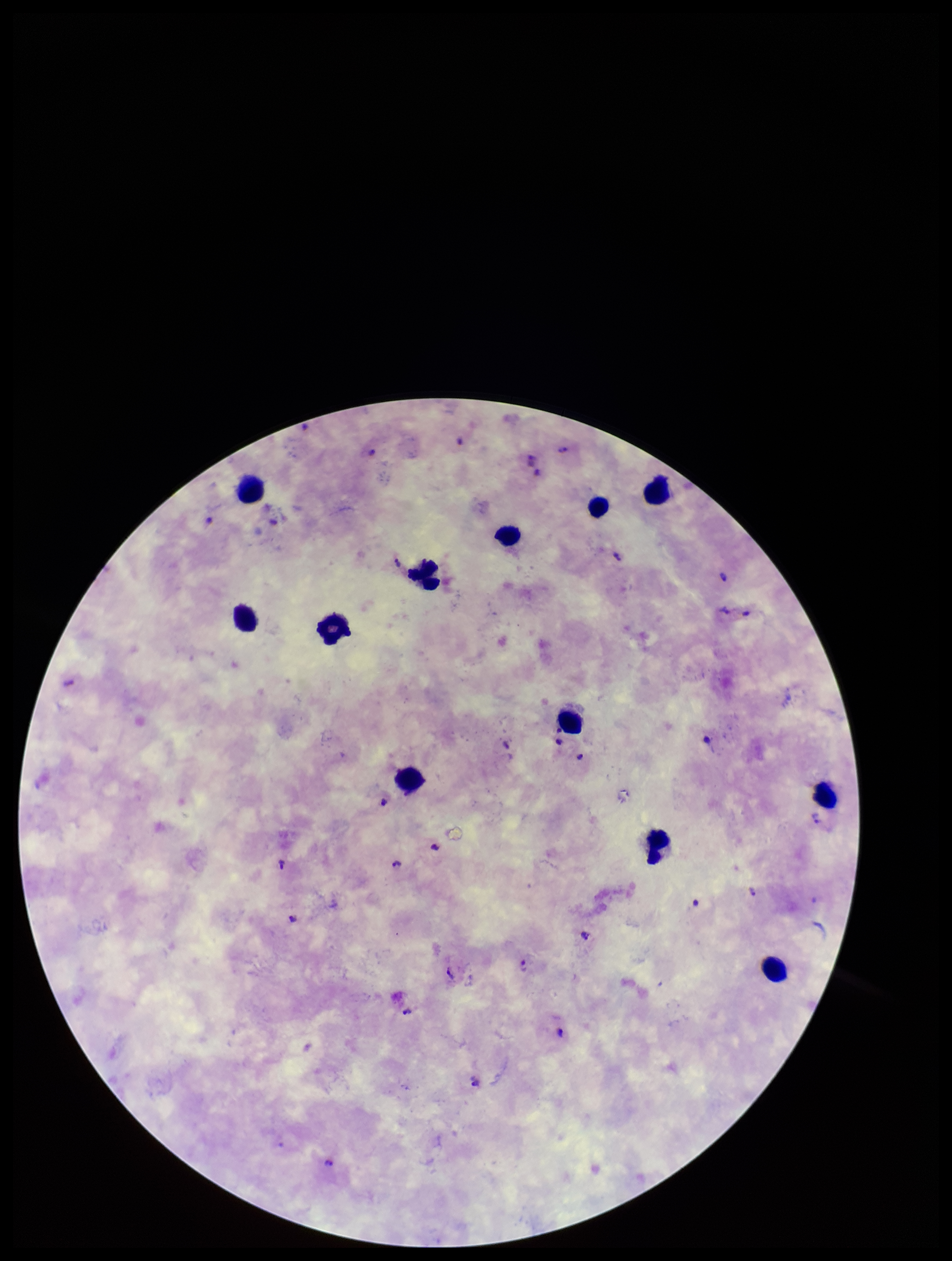

preparation = thick smear
field of view = single
capture = smartphone photograph through the microscope eyepiece
stain = Giemsa
parasite count = 21
leukocyte count = 12
image size = 952×1261 pixels
species reported for this patient = Plasmodium falciparum
Plasmodium parasites = detected
patient malaria status = infected